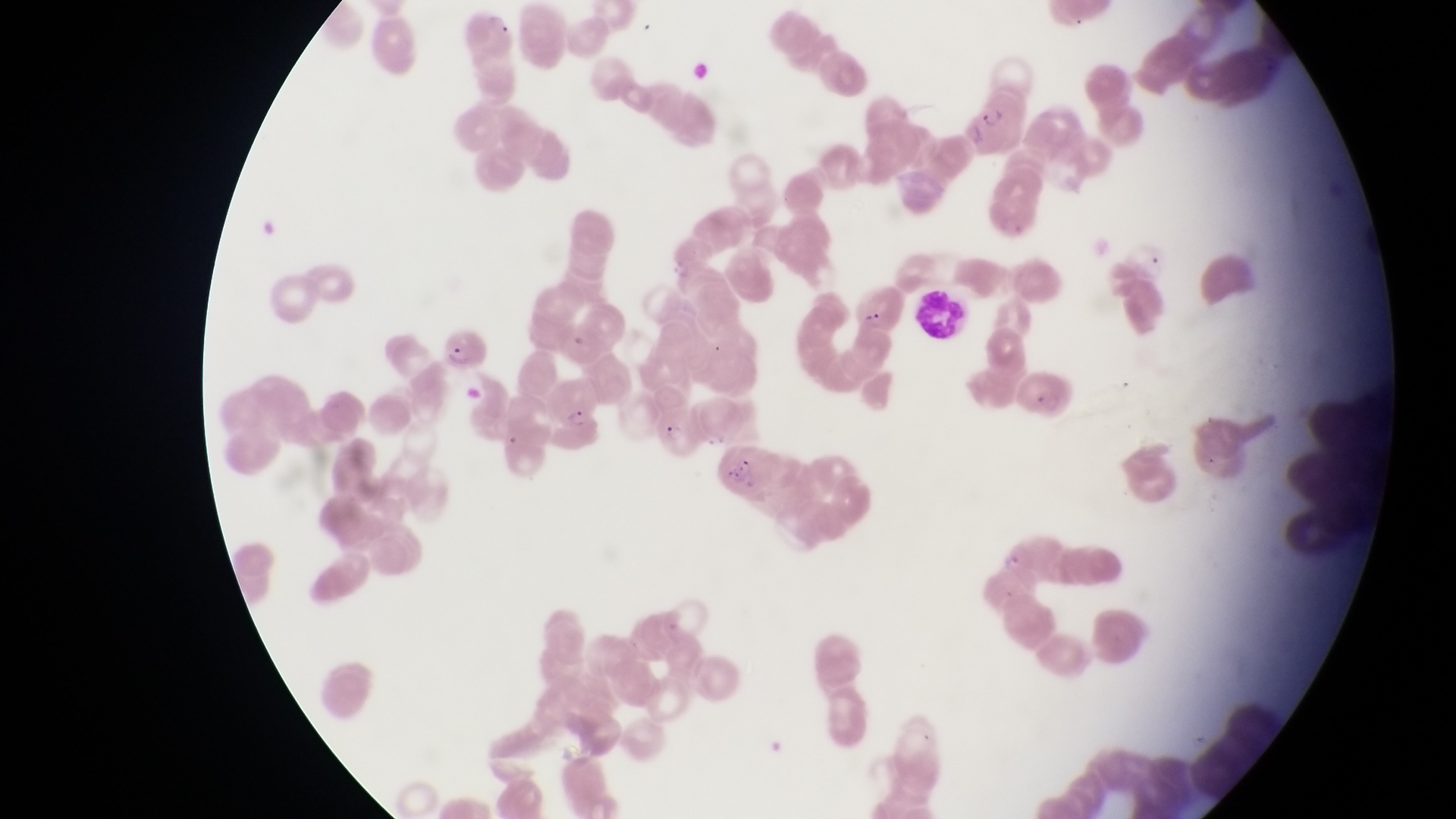
country: Uganda
parasitised_red_blood_cell_locations: 'approximate bounding boxes as {left, top, right, bottom} in pixels: {956, 86, 1023, 155}, {439, 323, 488, 373}, {1014, 369, 1075, 422}, {545, 377, 597, 426}, {655, 404, 700, 457}, {710, 441, 776, 501}'
magnification: 1000x
leukocyte_locations: 'approximate bounding boxes as {left, top, right, bottom} in pixels: {912, 285, 968, 346}'
trophozoite_locations: 'approximate bounding boxes as {left, top, right, bottom} in pixels: {1138, 245, 1171, 281}'
image_size: 1456×819 pixels
capture: smartphone photograph through the eyepiece of an Olympus CX-23 microscope
field_of_view: single
preparation: thin blood film